Identify the parasite.
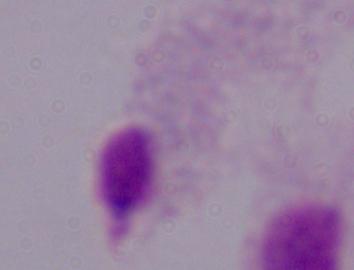
A trichomonad.

magnification = 1000x
modality = micrograph